Name the parasite shown.
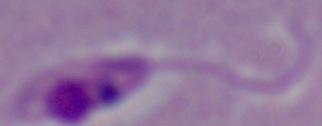
Leishmania.

Summary:
  - Magnification: 1000x
  - Modality: micrograph